State which parasite is depicted.
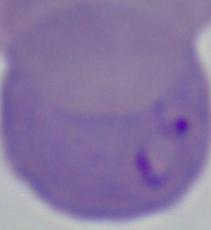

This is Babesia.

Captured at 1000x magnification. Micrograph.